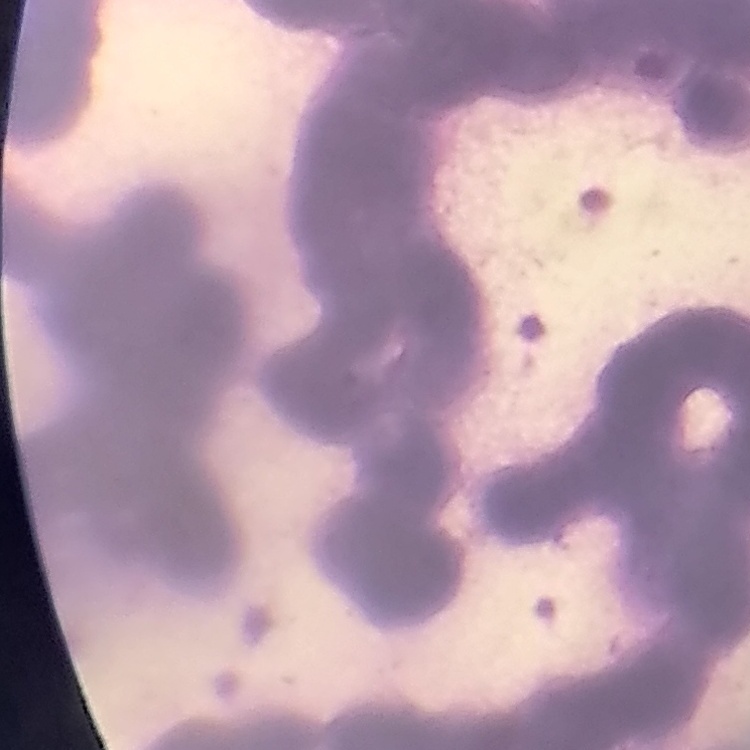 The erythrocytes exhibit rouleaux formation. Field's or Giemsa stain. Thin blood smear. Square crop of a larger photomicrograph.